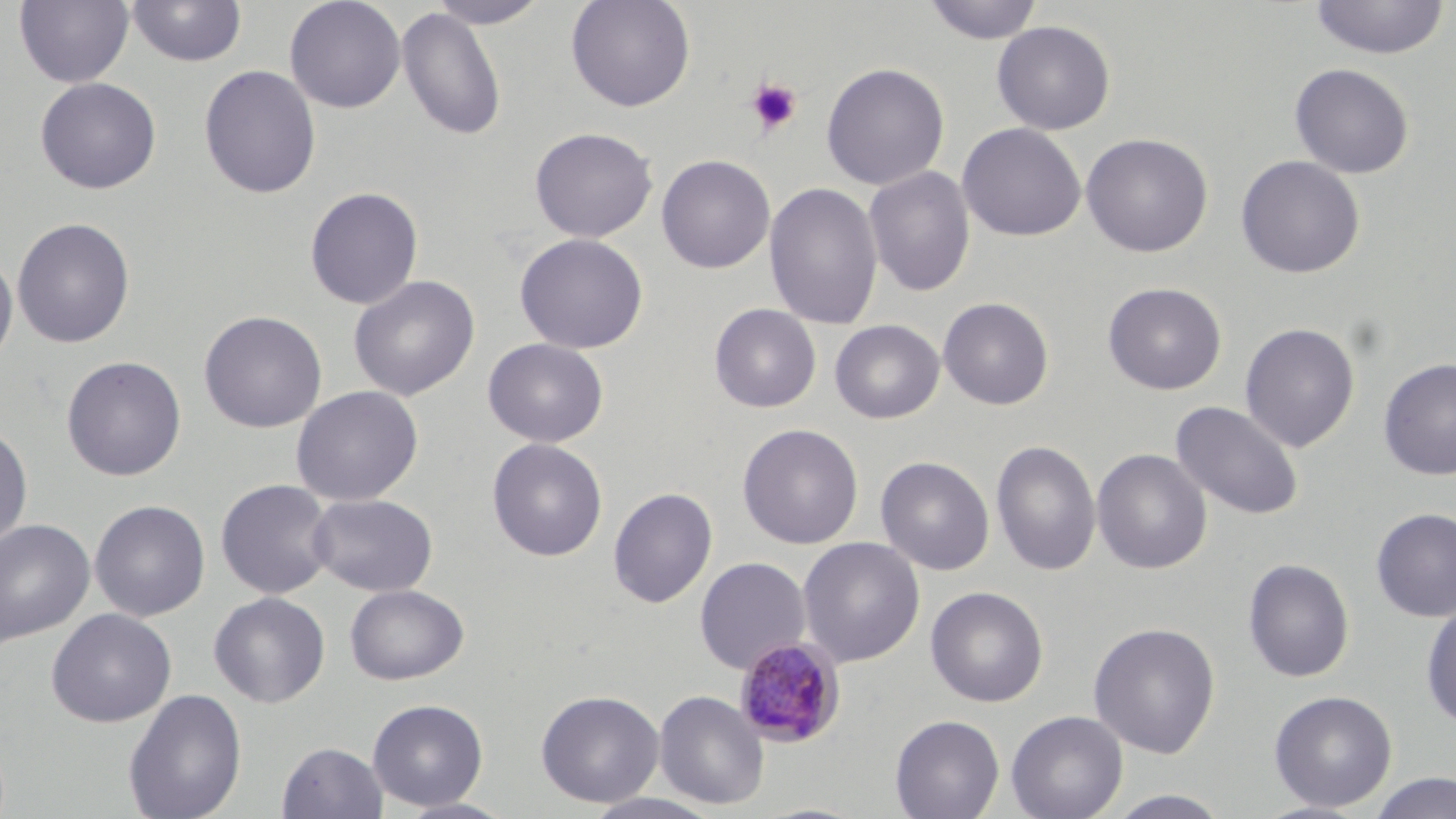
Summary:
  - Coordinate format: approximate bounding boxes as (x1,y1)-(x2,y2) corner pairs in pixels
  - Platelet locations: (745,77)-(803,136)
  - Plasmodium malariae-infected red blood cell locations: (734,636)-(847,748)
  - Uninfected red blood cell locations: (15,0)-(134,88), (126,0)-(247,68), (284,0)-(406,113), (426,0)-(553,29), (566,0)-(696,112), (922,0)-(1044,45), (1309,1)-(1450,60), (397,6)-(507,142), (992,20)-(1116,135), (821,61)-(950,190), (1289,63)-(1414,179), (199,64)-(321,199), (35,76)-(161,195), (957,123)-(1086,242), (530,127)-(657,243), (1080,132)-(1213,257), (656,154)-(775,274), (1236,155)-(1365,279), (864,165)-(975,296), (764,181)-(883,331), (304,186)-(424,309), (12,217)-(135,348), (514,233)-(648,354), (0,251)-(18,370), (348,275)-(480,401), (1103,282)-(1226,395), (938,297)-(1054,410), (709,304)-(821,413), (198,310)-(327,434), (830,319)-(945,424), (1239,322)-(1360,453), (482,338)-(609,447), (61,355)-(187,481), (1377,358)-(1456,480), (291,385)-(424,506), (1170,400)-(1305,521), (0,423)-(33,552), (737,423)-(863,549), (487,438)-(608,562), (991,439)-(1102,577), (1092,448)-(1212,575), (875,456)-(994,575), (216,479)-(336,599), (607,487)-(718,608), (307,493)-(438,597), (89,500)-(211,621), (1371,507)-(1456,621), (0,518)-(96,646), (797,536)-(925,668), (694,556)-(811,673), (1242,558)-(1355,683), (344,583)-(469,685), (925,586)-(1048,707), (209,592)-(330,708), (1421,600)-(1456,730), (46,608)-(176,727), (1088,622)-(1221,758), (123,689)-(247,819), (536,690)-(664,807), (654,690)-(769,810), (1268,690)-(1397,811), (367,698)-(488,811), (1006,710)-(1128,819), (889,714)-(1005,819), (277,741)-(388,819), (1365,772)-(1456,818), (1104,789)-(1234,819), (580,792)-(725,819), (394,798)-(518,818)
  - Slide-level diagnosis: Plasmodium malariae
  - Field of view: one of a larger specimen
  - Stain: May-Grünwald-Giemsa
  - Preparation: thin blood film
  - Modality: light microscopy
  - Image size: 1456×819 pixels
  - Magnification: 1000x